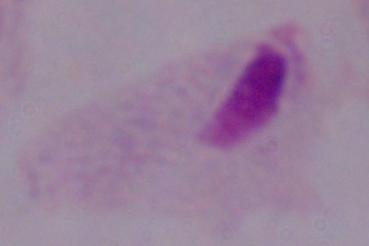 Photomicrograph. A trichomonad is shown. 1000x magnification.